Outline each blood parasite and name the species.
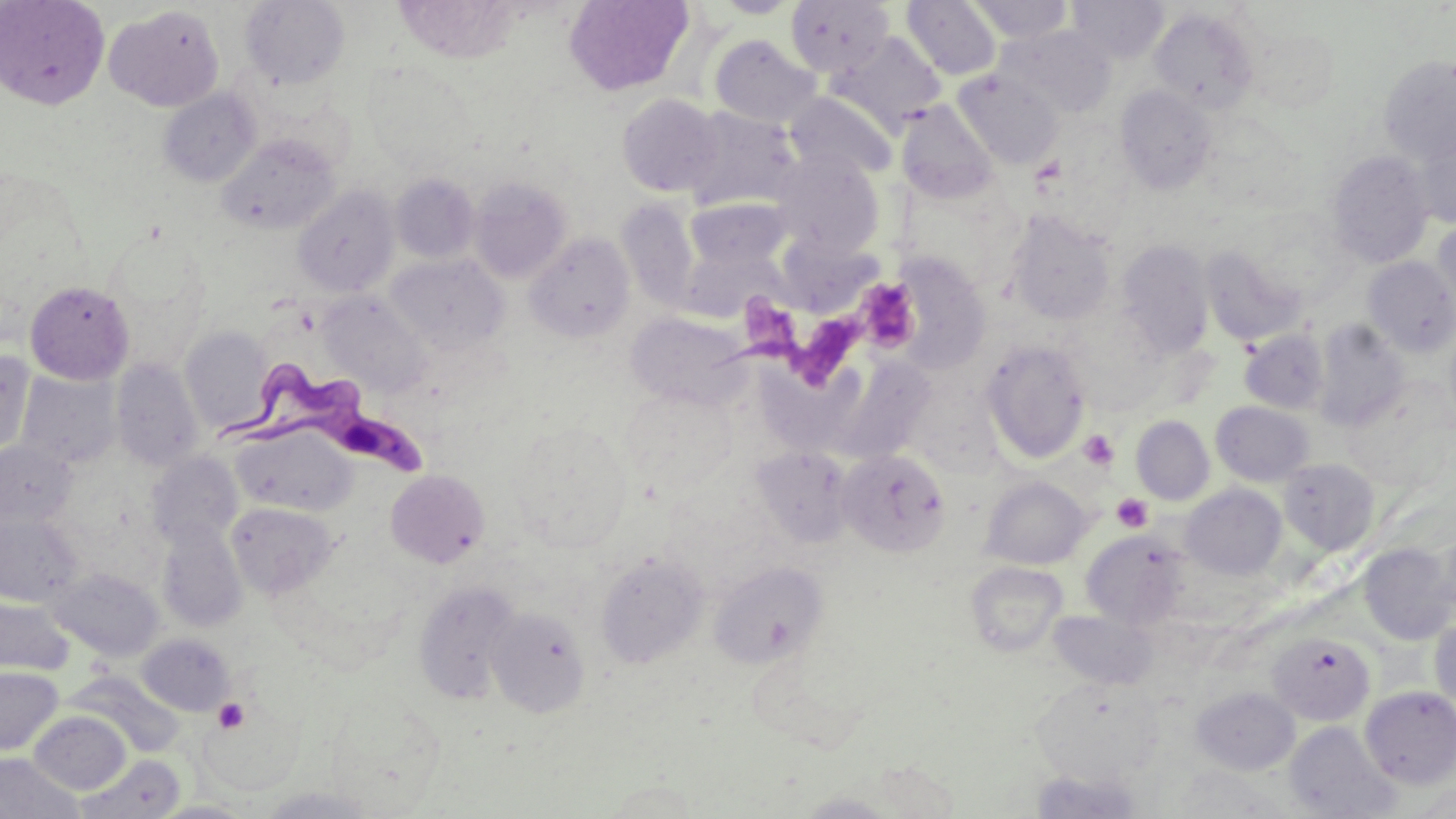

Approximate bounding boxes as (x1, y1, x2, y2) in pixels.
Trypanosoma brucei: (221, 364, 429, 481).
No Plasmodium falciparum, Plasmodium ovale, Plasmodium malariae, Plasmodium vivax, or Babesia divergens observed.

slide-level diagnosis = Trypanosoma brucei
field of view = single
platelet locations = approximate bounding boxes as (x1, y1, x2, y2) in pixels: (858, 277, 918, 353), (743, 303, 859, 384), (1078, 430, 1120, 472), (1111, 493, 1153, 533), (213, 698, 249, 733)
image size = 1456×819 pixels
uninfected red blood cell locations = approximate bounding boxes as (x1, y1, x2, y2) in pixels: (0, 0, 110, 110), (563, 0, 694, 95), (712, 0, 803, 18), (966, 0, 1075, 44), (1067, 0, 1169, 62), (239, 1, 350, 90), (784, 1, 895, 77), (902, 1, 1002, 81), (105, 4, 225, 111), (1148, 6, 1261, 114), (997, 25, 1117, 118), (1245, 26, 1341, 112), (830, 32, 947, 134), (708, 34, 822, 129), (1378, 58, 1456, 165), (953, 70, 1063, 169), (1116, 84, 1217, 195), (158, 88, 261, 187), (785, 92, 897, 182), (617, 93, 724, 197), (896, 100, 999, 204), (683, 106, 802, 212), (1414, 124, 1456, 229), (217, 134, 340, 235), (772, 151, 885, 255), (1327, 151, 1434, 268), (391, 173, 480, 263), (468, 176, 573, 283), (293, 185, 400, 298), (685, 197, 790, 271), (616, 198, 702, 313), (1005, 209, 1118, 327), (1431, 218, 1456, 324), (524, 232, 635, 343), (1115, 238, 1214, 357), (778, 239, 882, 310), (679, 242, 789, 322), (1200, 246, 1303, 346), (887, 252, 992, 373), (386, 253, 509, 353), (1364, 257, 1456, 358), (25, 280, 134, 384), (317, 291, 431, 397), (625, 311, 751, 409), (1312, 319, 1410, 432), (180, 326, 274, 433), (1239, 330, 1329, 414), (981, 338, 1091, 463), (0, 351, 36, 457), (823, 353, 938, 466), (111, 359, 204, 469), (755, 366, 867, 451), (17, 371, 122, 469), (620, 385, 737, 498), (1211, 401, 1315, 486), (1131, 416, 1214, 505), (509, 420, 632, 551), (232, 425, 356, 516), (0, 440, 77, 528), (750, 446, 855, 548), (836, 449, 951, 557), (146, 451, 243, 547), (1278, 458, 1379, 555), (385, 469, 489, 567), (981, 476, 1091, 569), (1181, 484, 1286, 580), (226, 502, 339, 599), (0, 514, 84, 607), (156, 520, 247, 633), (1081, 529, 1190, 629), (1430, 530, 1456, 625), (1359, 542, 1455, 645), (594, 551, 709, 668), (708, 560, 829, 667), (965, 561, 1068, 658), (50, 568, 163, 661), (412, 579, 521, 704), (0, 597, 74, 676), (486, 606, 590, 717), (1046, 610, 1159, 691), (1429, 618, 1456, 711), (1268, 632, 1374, 725), (138, 633, 236, 715), (0, 666, 63, 755), (70, 671, 181, 758), (1031, 677, 1164, 786), (1192, 686, 1300, 775), (1360, 686, 1456, 789), (30, 711, 130, 794), (1284, 721, 1401, 819), (0, 752, 83, 819), (77, 755, 184, 819), (1162, 766, 1292, 817), (1029, 767, 1142, 818), (602, 780, 702, 817), (1408, 783, 1456, 815), (256, 785, 382, 818), (794, 791, 901, 818), (150, 800, 257, 818)
magnification = 1000x
stain = May-Grünwald-Giemsa
modality = light microscopy
preparation = thin blood film